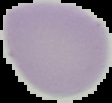
image type = segmented cell region with the area outside set to black
result = no Plasmodium parasites detected
preparation = thin blood smear
image size = 112×103 pixels